State the preparation type.
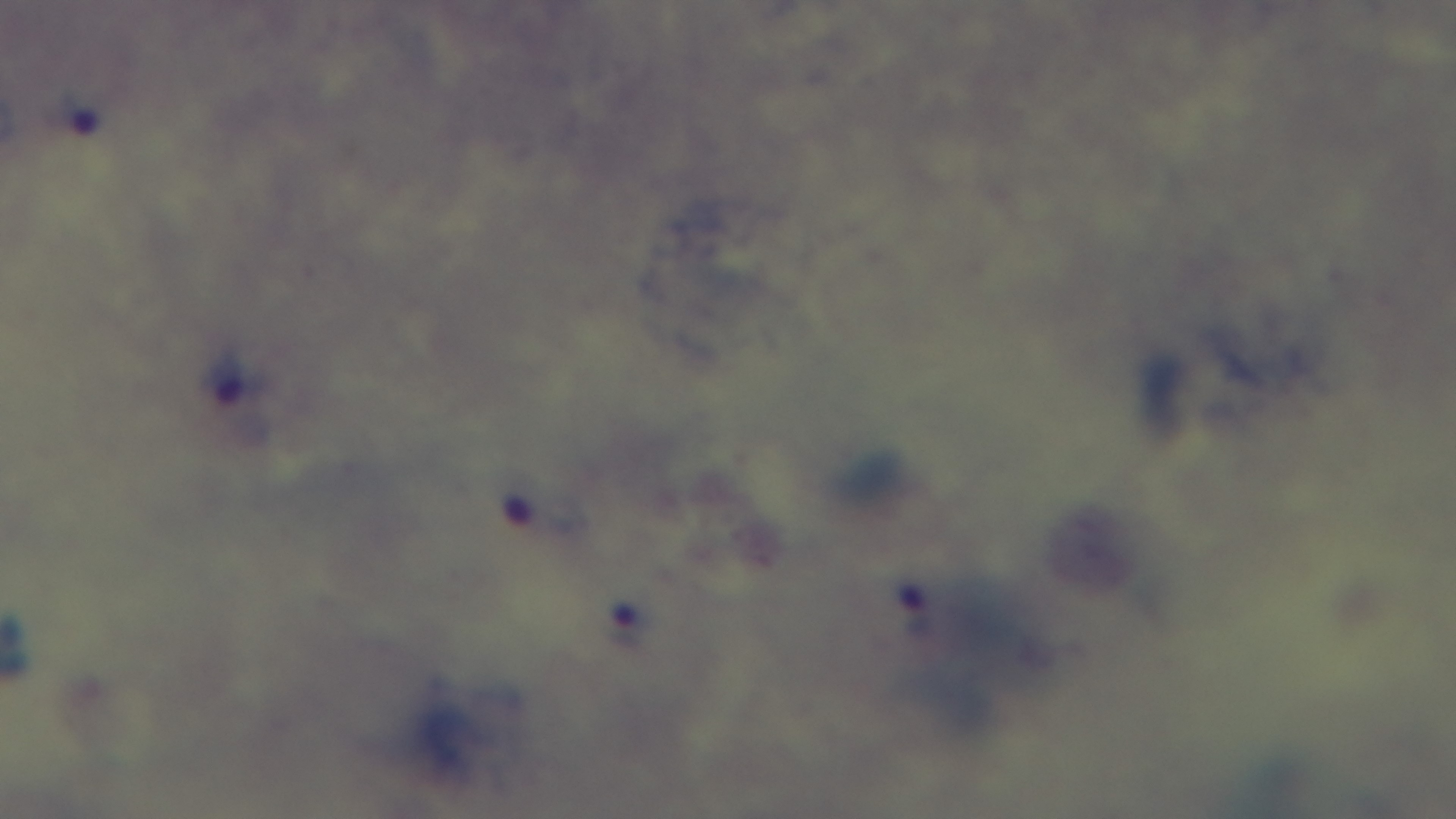
A thick smear.

Summary:
  - Modality: light microscopy
  - Malaria status: infected
  - Objective: 100x oil immersion
  - Capture: mounted 4K digital camera
  - Field of view: one from the slide
  - Stain: Giemsa